Describe the morphology of the red blood cells.
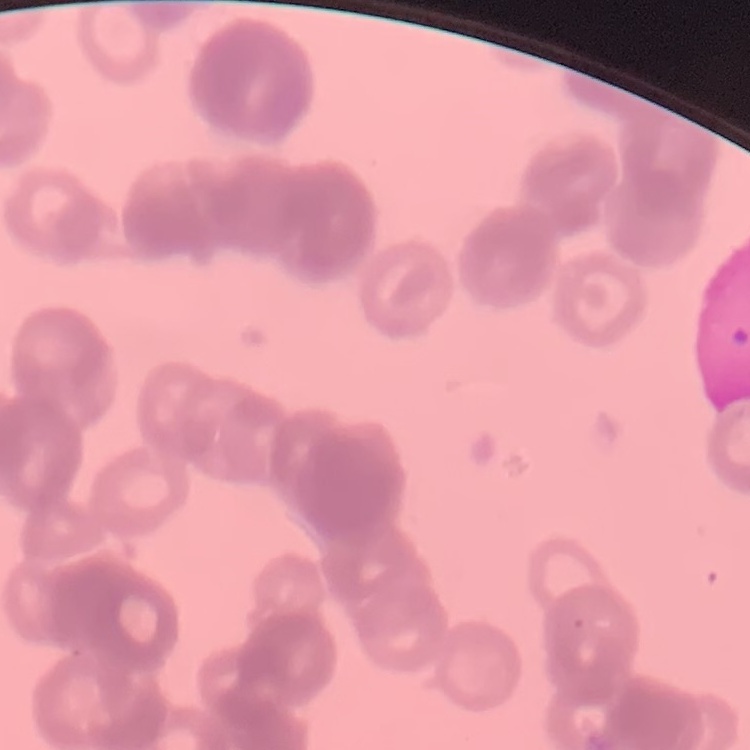

Rouleaux formation.

Summary:
  - Preparation: thin blood film
  - Stain: Field's or Giemsa
  - Image type: square crop of a larger photomicrograph